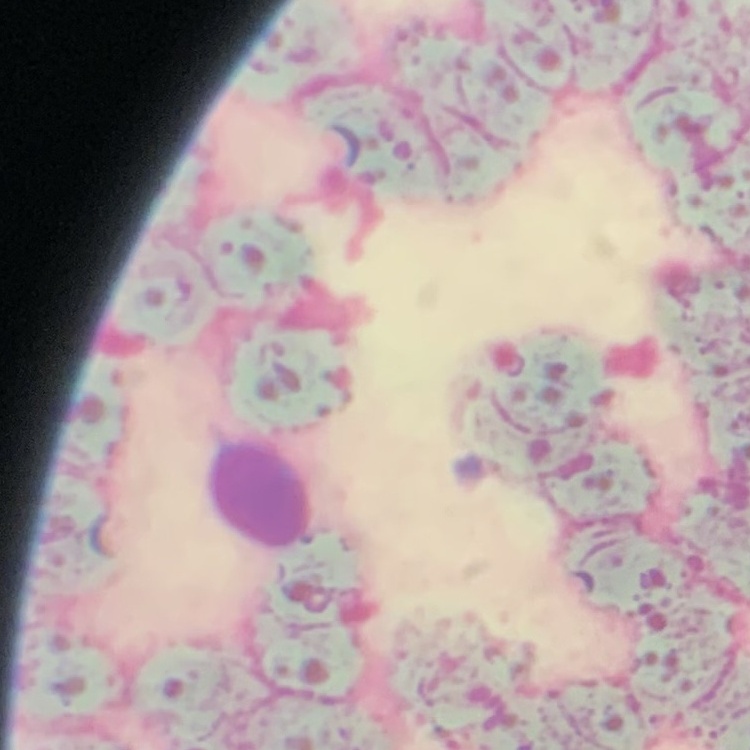

The red blood cells show rouleaux formation. Thin peripheral smear. Square crop of a larger photomicrograph. Field's or Giemsa stain.